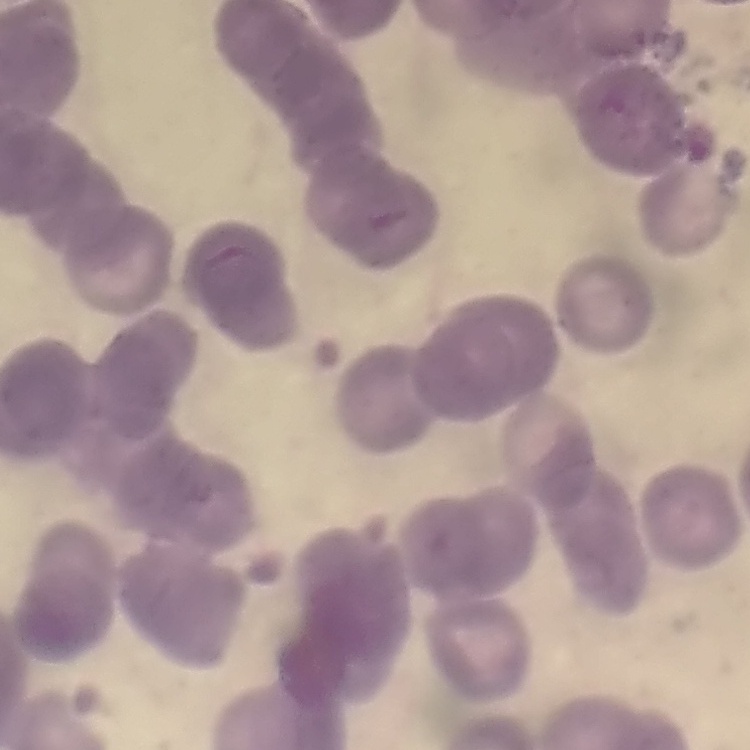
erythrocyte_morphology: rouleaux formation
preparation: thin peripheral smear
image_type: square crop of a larger photomicrograph
stain: Field's or Giemsa